Comment on the morphology of the red blood cells.
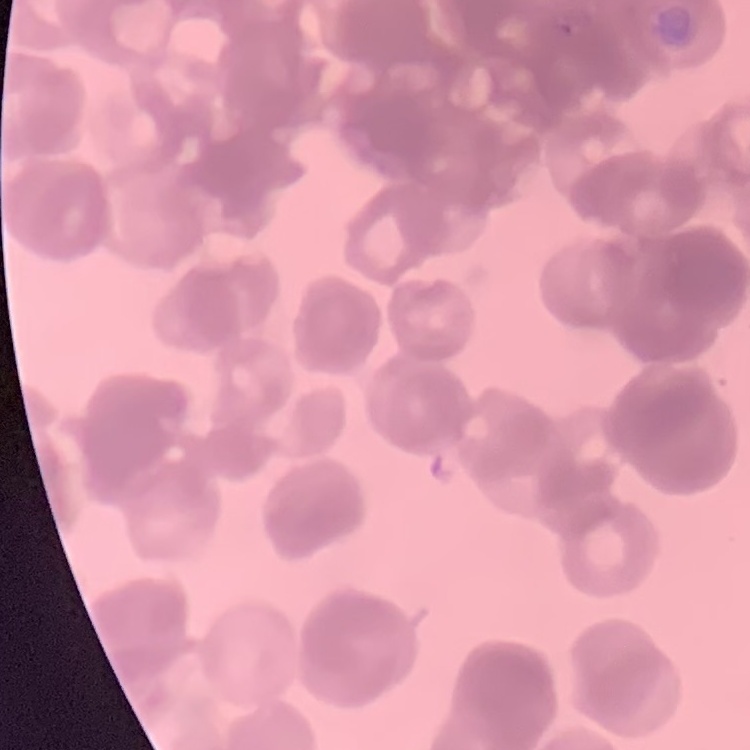
They show rouleaux formation.

Stained with either Field's or Giemsa. One tile cut from a larger photomicrograph. Thin blood smear.